Report the malaria status of this cell.
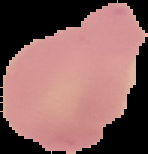
Uninfected.

image_size: 148×154 pixels
preparation: thin blood smear
image_type: segmented cell region with the area outside set to black